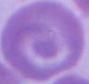

A red blood cell is seen. Captured at 1000x magnification. Photomicrograph.